Assess this cell for malaria.
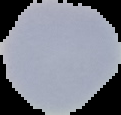

Uninfected.

Summary:
  - Image size: 121×115 pixels
  - Image type: segmented cell region with the area outside set to black
  - Preparation: thin blood smear